Name the blood parasite species.
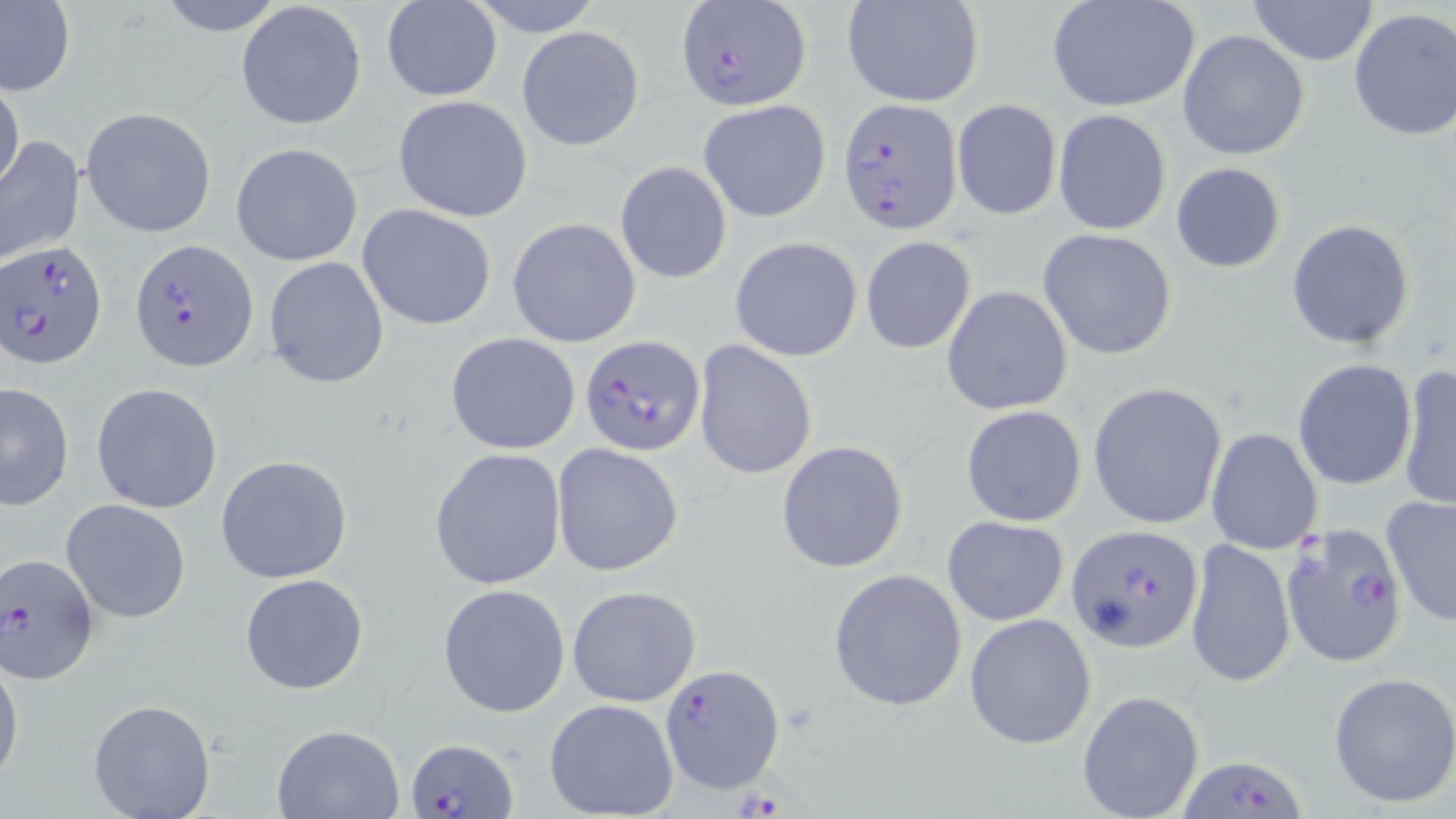
Plasmodium falciparum.

Approximate bounding boxes as [x1, y1, x2, y2] in pixels. Plasmodium falciparum-infected red blood cell locations: [673, 4, 812, 111], [836, 97, 960, 231], [1, 239, 106, 369], [131, 241, 257, 370], [580, 338, 707, 455], [1279, 521, 1406, 667], [1062, 527, 1200, 655], [1, 552, 101, 685], [659, 662, 785, 795], [406, 737, 518, 817], [1180, 752, 1308, 818]. Uninfected red blood cell locations: [156, 0, 285, 36], [470, 0, 603, 35], [841, 0, 987, 108], [1046, 0, 1202, 114], [1246, 0, 1380, 67], [381, 1, 503, 103], [0, 2, 76, 96], [236, 2, 367, 131], [1347, 8, 1456, 142], [516, 25, 647, 152], [1178, 30, 1310, 161], [0, 80, 25, 196], [392, 94, 534, 221], [697, 99, 832, 224], [951, 99, 1061, 221], [80, 106, 218, 237], [1053, 109, 1171, 236], [0, 135, 86, 267], [230, 141, 363, 267], [614, 161, 732, 283], [1171, 162, 1287, 274], [358, 202, 498, 331], [506, 218, 641, 348], [1285, 218, 1416, 350], [1037, 228, 1178, 360], [729, 235, 863, 360], [860, 236, 976, 354], [263, 255, 389, 389], [941, 286, 1073, 415], [445, 332, 581, 454], [693, 340, 818, 481], [1292, 360, 1416, 488], [1396, 364, 1456, 511], [0, 382, 75, 511], [91, 383, 223, 514], [1088, 383, 1226, 529], [960, 404, 1087, 527], [1206, 428, 1323, 555], [775, 439, 910, 575], [552, 443, 684, 578], [428, 447, 568, 591], [216, 454, 353, 584], [1380, 496, 1455, 629], [61, 498, 192, 623], [942, 515, 1069, 626], [1185, 536, 1297, 690], [828, 568, 967, 712], [240, 572, 370, 695], [438, 583, 570, 718], [567, 585, 702, 708], [963, 613, 1096, 748], [0, 651, 24, 792], [1328, 671, 1456, 810], [1077, 689, 1205, 818], [87, 699, 216, 819], [543, 699, 679, 819], [271, 723, 407, 817]. 1000x magnification. Light microscopy. Thin blood film. May-Grünwald-Giemsa-stained preparation. Single field of view. Image is 1456×819 pixels.